Evaluate for malaria.
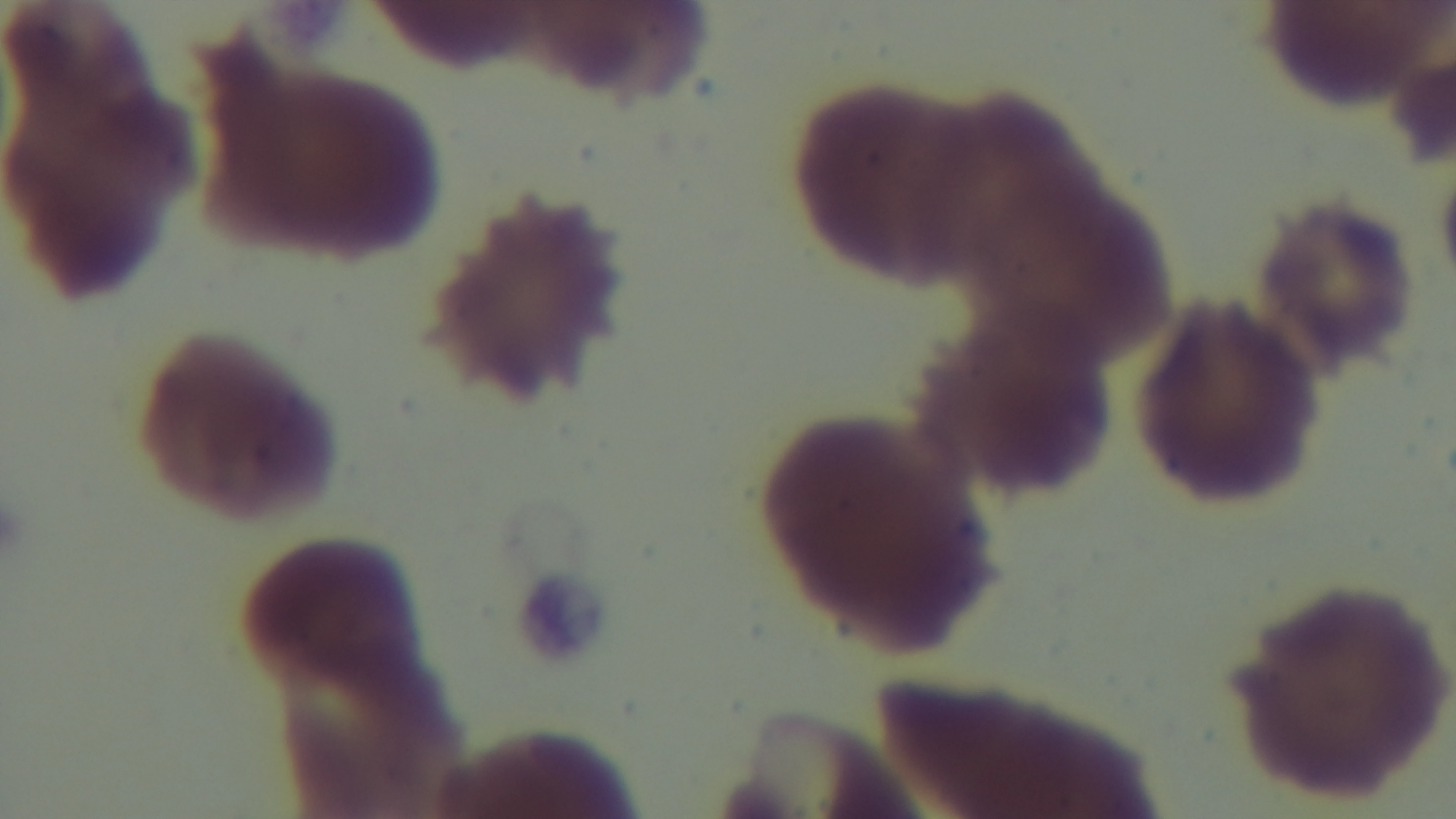

It is uninfected.

Summary:
  - Preparation: thin
  - Objective: 100x oil immersion
  - Stain: Giemsa
  - Capture: mounted 4K digital camera
  - Modality: light microscopy
  - Field of view: single